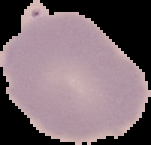
image size = 151×145 pixels
preparation = thin blood smear
image type = segmented cell region on a black background
malaria status = uninfected